Name the cell type shown.
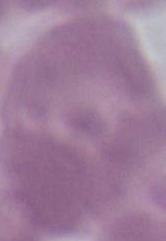
An erythrocyte.

Photomicrograph. Captured at 1000x magnification.